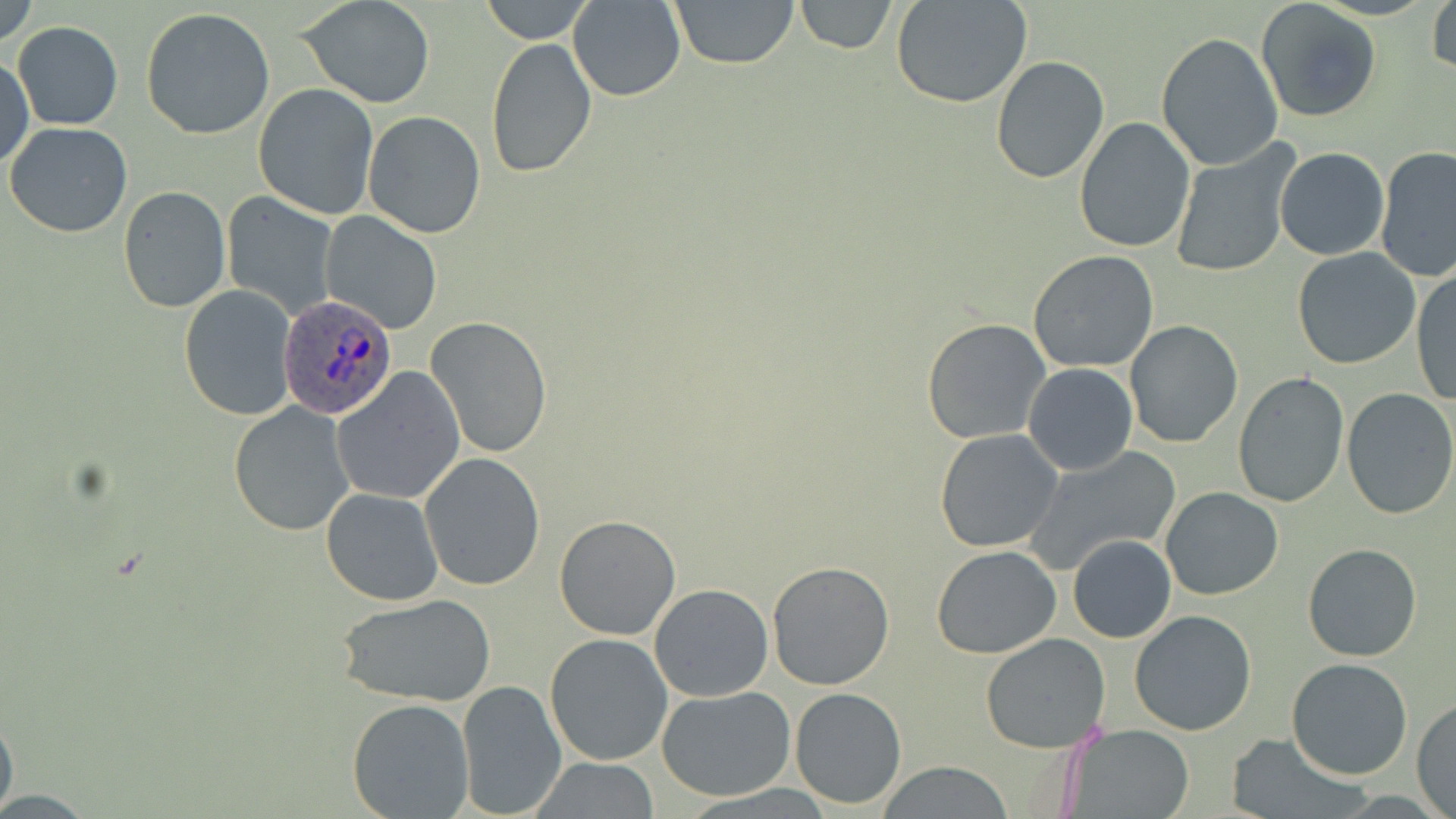

{
  "slide_level_diagnosis": "Plasmodium ovale",
  "field_of_view": "one of a larger specimen",
  "image_size": "1456×819 pixels",
  "uninfected_red_blood_cell_locations": "approximate bounding boxes as named x1/y1/x2/y2 corners in pixels: (x1=0, y1=0, x2=39, y2=49), (x1=297, y1=0, x2=437, y2=110), (x1=478, y1=0, x2=594, y2=44), (x1=569, y1=0, x2=686, y2=102), (x1=669, y1=0, x2=800, y2=70), (x1=792, y1=0, x2=897, y2=53), (x1=1256, y1=0, x2=1383, y2=122), (x1=1427, y1=0, x2=1455, y2=78), (x1=893, y1=1, x2=1032, y2=109), (x1=141, y1=8, x2=277, y2=140), (x1=12, y1=21, x2=123, y2=131), (x1=1156, y1=33, x2=1284, y2=171), (x1=483, y1=37, x2=598, y2=178), (x1=0, y1=50, x2=33, y2=172), (x1=990, y1=56, x2=1110, y2=184), (x1=252, y1=83, x2=380, y2=220), (x1=363, y1=111, x2=487, y2=240), (x1=1074, y1=117, x2=1197, y2=252), (x1=4, y1=121, x2=132, y2=237), (x1=1168, y1=142, x2=1297, y2=279), (x1=1375, y1=146, x2=1456, y2=282), (x1=1276, y1=147, x2=1389, y2=260), (x1=117, y1=186, x2=231, y2=314), (x1=222, y1=191, x2=340, y2=320), (x1=319, y1=212, x2=444, y2=334), (x1=1292, y1=248, x2=1421, y2=369), (x1=1027, y1=250, x2=1159, y2=373), (x1=1410, y1=266, x2=1456, y2=409), (x1=179, y1=286, x2=297, y2=421), (x1=427, y1=317, x2=552, y2=457), (x1=920, y1=318, x2=1051, y2=445), (x1=1124, y1=320, x2=1245, y2=448), (x1=1023, y1=364, x2=1137, y2=475), (x1=332, y1=367, x2=463, y2=505), (x1=1232, y1=372, x2=1350, y2=508), (x1=1340, y1=387, x2=1456, y2=520), (x1=1034, y1=389, x2=1161, y2=535), (x1=228, y1=402, x2=354, y2=537), (x1=935, y1=428, x2=1064, y2=553), (x1=1025, y1=445, x2=1184, y2=578), (x1=418, y1=453, x2=546, y2=593), (x1=1160, y1=487, x2=1285, y2=600), (x1=321, y1=488, x2=445, y2=606), (x1=554, y1=514, x2=682, y2=641), (x1=1067, y1=534, x2=1177, y2=643), (x1=1303, y1=543, x2=1422, y2=662), (x1=932, y1=546, x2=1060, y2=659), (x1=766, y1=559, x2=895, y2=689), (x1=648, y1=583, x2=774, y2=702), (x1=334, y1=593, x2=495, y2=706), (x1=1129, y1=610, x2=1257, y2=736), (x1=544, y1=632, x2=674, y2=765), (x1=981, y1=632, x2=1112, y2=752), (x1=1286, y1=657, x2=1414, y2=780), (x1=456, y1=677, x2=568, y2=816), (x1=656, y1=685, x2=797, y2=800), (x1=790, y1=687, x2=905, y2=808), (x1=1412, y1=698, x2=1456, y2=816), (x1=347, y1=699, x2=474, y2=818), (x1=0, y1=705, x2=19, y2=819), (x1=1063, y1=725, x2=1196, y2=819), (x1=1225, y1=734, x2=1366, y2=817), (x1=528, y1=758, x2=662, y2=817), (x1=875, y1=764, x2=1016, y2=818)",
  "preparation": "thin blood smear",
  "plasmodium_ovale_infected_red_blood_cell_locations": "approximate bounding boxes as named x1/y1/x2/y2 corners in pixels: (x1=277, y1=295, x2=397, y2=418)",
  "stain": "May-Grünwald-Giemsa",
  "magnification": "1000x",
  "modality": "optical microscopy"
}